Classify this cell by malaria status.
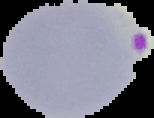

It is parasitized.

{
  "image_type": "cell region segmented out of the field of view; surrounding area masked to black",
  "preparation": "thin blood film",
  "image_size": "154×118 pixels"
}